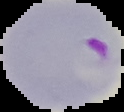
{
  "result": "Plasmodium parasites identified",
  "image_size": "124×112 pixels",
  "preparation": "thin blood film",
  "image_type": "cell region segmented out of the field of view; surrounding area masked to black"
}